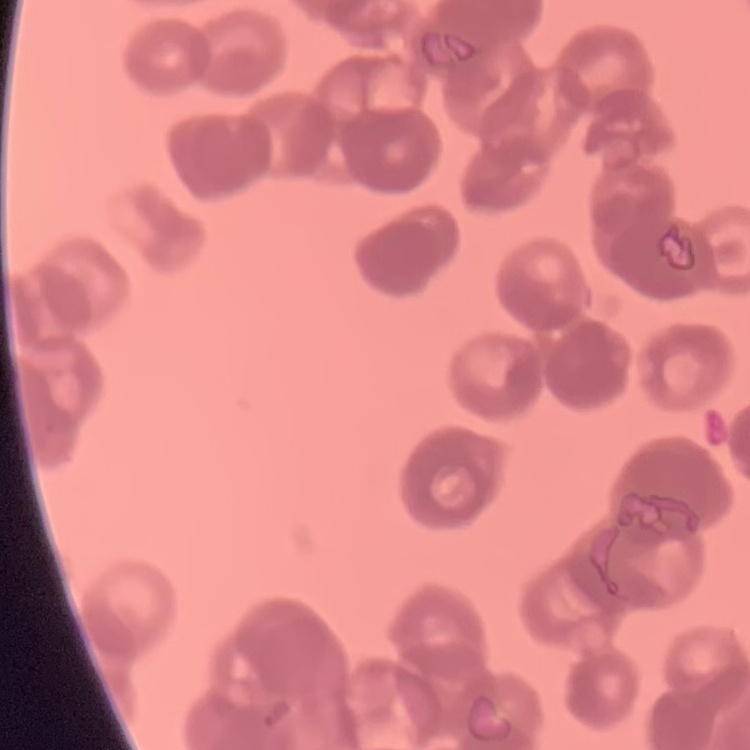
The red blood cells show rouleaux formation. Thin blood smear. One tile cut from a larger photomicrograph. Field's or Giemsa stain.